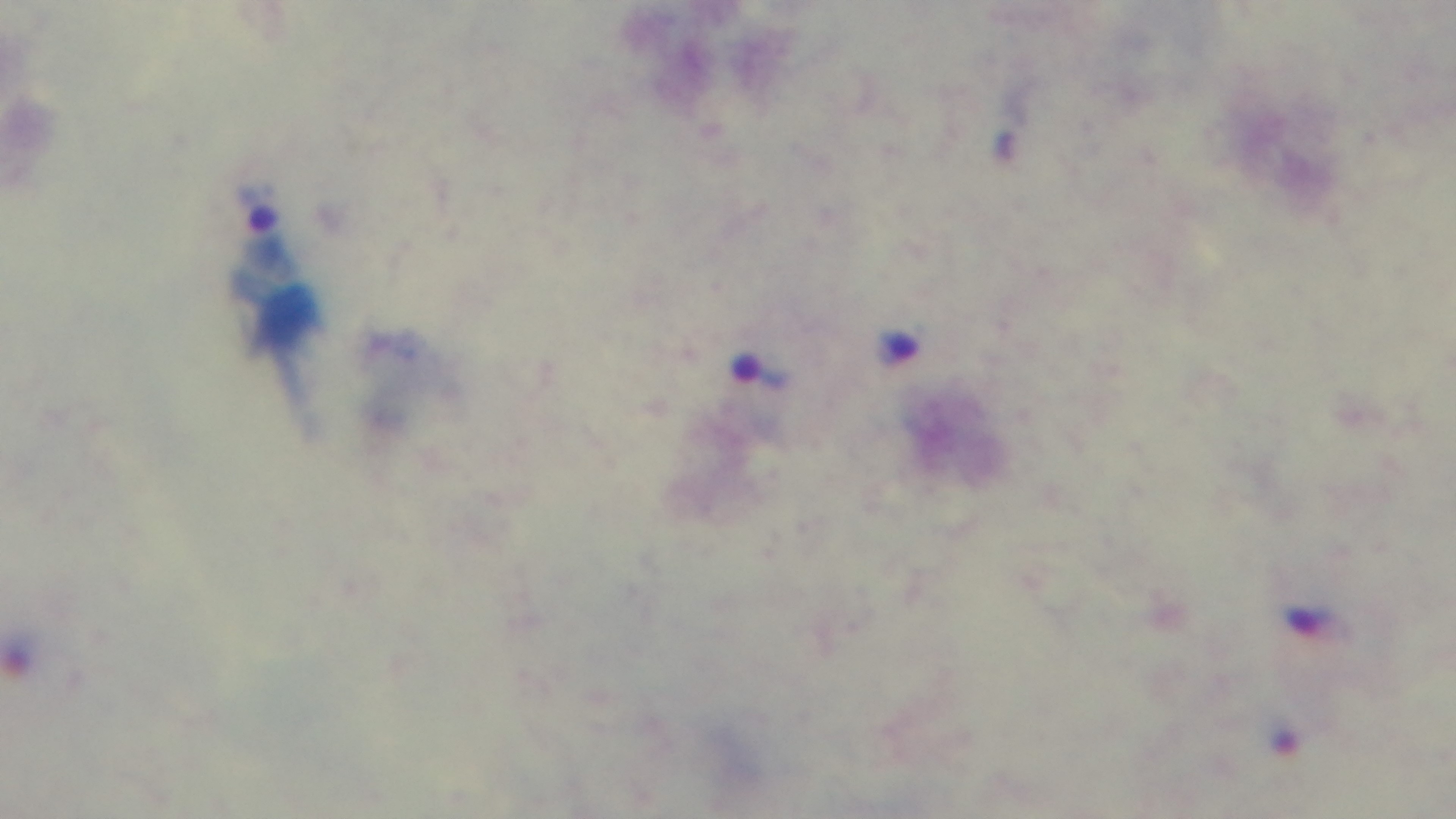

objective: 100x oil immersion
field_of_view: single
malaria_status: positive
modality: light microscopy
stain: Giemsa
capture: mounted 4K digital camera
preparation: thick blood film